Report the malaria status of this cell.
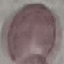

Uninfected.

Automatically extracted cell patch, resized to 64 × 64 pixels. Photographed with a smartphone camera at the microscope eyepiece. Thin smear of blood. Giemsa-stained preparation.